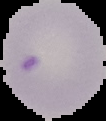
{
  "preparation": "thin blood film",
  "image_type": "segmented cell region with the area outside set to black",
  "malaria_status": "uninfected",
  "image_size": "106×121 pixels"
}